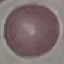
Summary:
  - Result: no malaria parasites seen
  - Preparation: thin blood smear
  - Capture: smartphone through the microscope eyepiece
  - Image type: cell patch, automatically extracted from a larger field of view and resized to 64 × 64 pixels
  - Stain: Giemsa